State which parasite is depicted.
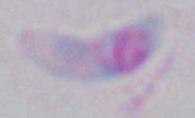
Toxoplasma gondii.

1000x magnification. Micrograph.